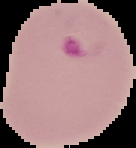

Summary:
  - Malaria status: parasitized
  - Image size: 136×148 pixels
  - Image type: segmented cell region on a black background
  - Preparation: thin blood smear